Comment on the morphology of the red blood cells.
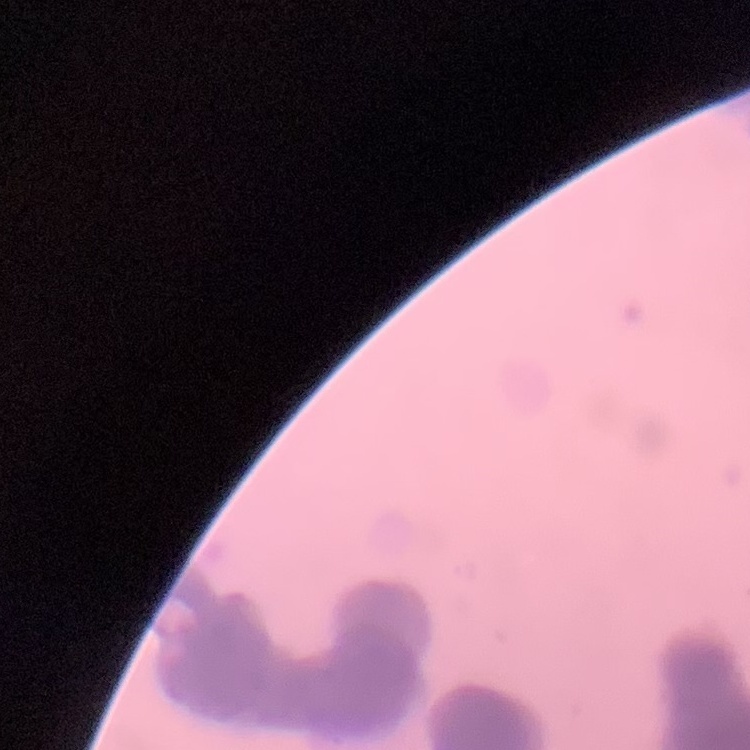

They show rouleaux formation.

Summary:
  - Preparation: thin peripheral smear
  - Image type: one tile cut from a larger photomicrograph
  - Stain: Field's or Giemsa